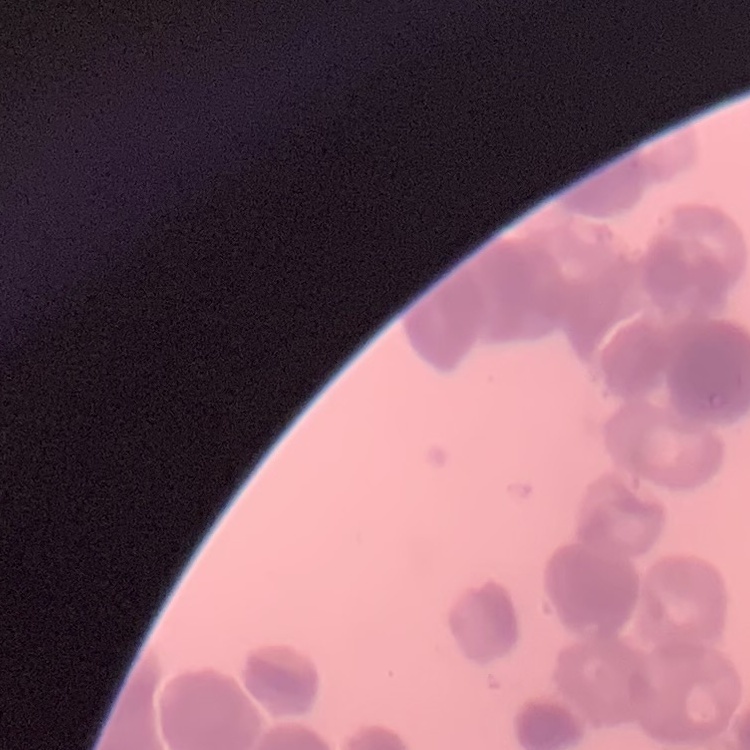 The red blood cells show rouleaux formation. Thin peripheral smear. Stained with either Field's or Giemsa. Square crop of a larger photomicrograph.